Locate every uninfected red blood cell.
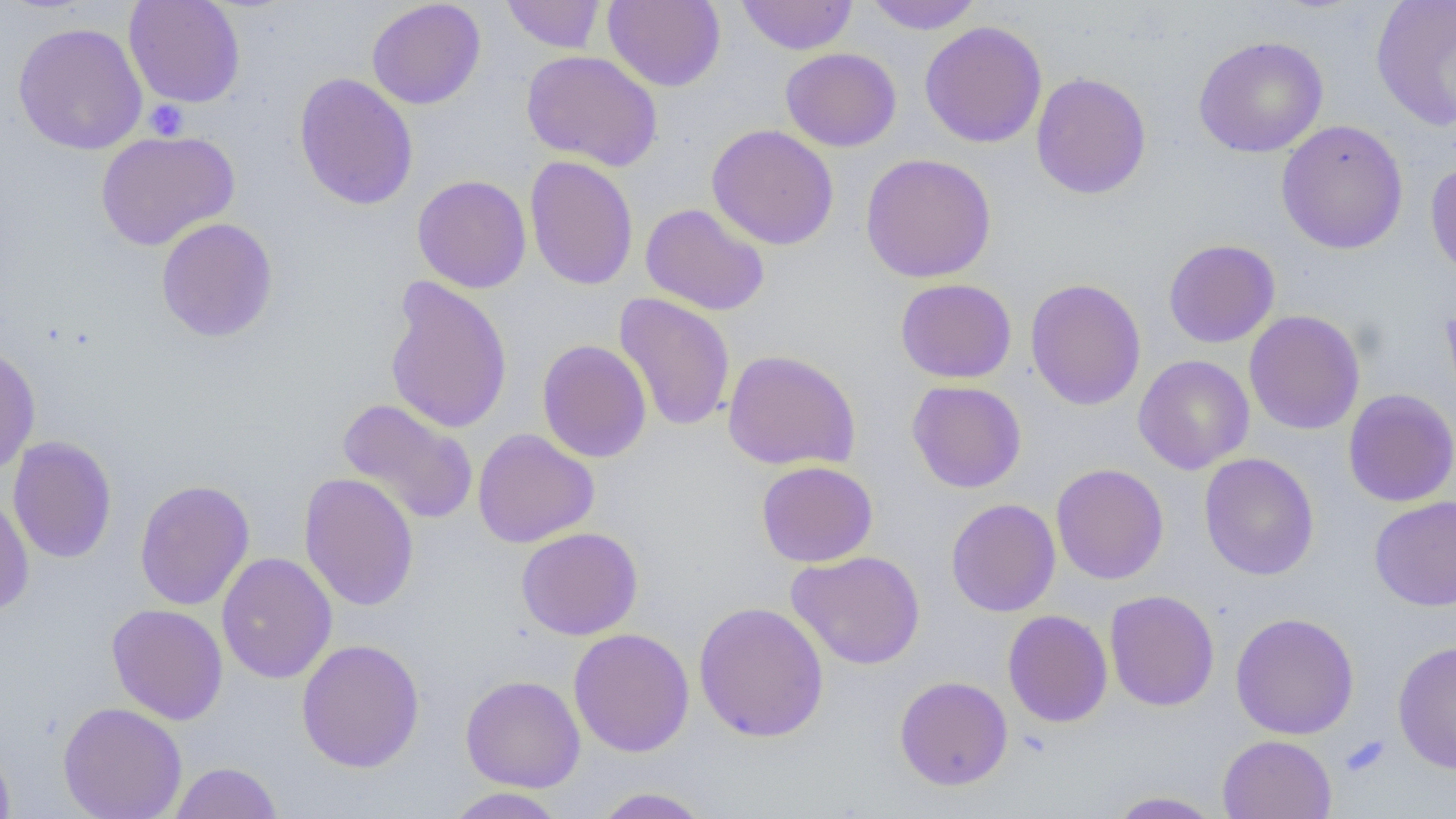
Approximate bounding boxes as (x1, y1, x2, y2) in pixels.
Uninfected red blood cells: (123, 0, 246, 108), (367, 0, 486, 110), (501, 0, 606, 53), (603, 0, 725, 91), (737, 0, 857, 55), (863, 0, 984, 34), (1370, 0, 1456, 133), (919, 20, 1047, 148), (12, 22, 148, 155), (1193, 35, 1328, 158), (780, 48, 902, 152), (521, 50, 663, 171), (1031, 71, 1152, 199), (294, 72, 419, 210), (1276, 119, 1409, 255), (707, 124, 839, 250), (95, 129, 240, 251), (859, 153, 997, 283), (524, 156, 638, 291), (1424, 160, 1456, 283), (412, 175, 531, 293), (640, 203, 771, 316), (155, 218, 279, 342), (1163, 238, 1280, 348), (384, 275, 514, 435), (895, 278, 1017, 383), (1025, 278, 1146, 410), (614, 292, 736, 432), (1244, 309, 1366, 435), (536, 339, 652, 463), (0, 345, 41, 475), (722, 349, 861, 471), (1133, 355, 1254, 474), (906, 380, 1027, 493), (1342, 389, 1456, 507), (337, 398, 479, 525), (472, 428, 599, 548), (7, 436, 118, 564), (1199, 453, 1319, 580), (756, 460, 878, 567), (1050, 463, 1169, 584), (299, 472, 419, 612), (134, 478, 255, 611), (0, 492, 35, 616), (1369, 495, 1456, 611), (946, 498, 1061, 617), (516, 527, 643, 640), (786, 550, 926, 670), (216, 552, 337, 685), (1104, 589, 1219, 711), (694, 601, 829, 742), (106, 604, 229, 725), (1003, 609, 1113, 728), (1230, 611, 1359, 740), (568, 628, 695, 757), (296, 639, 425, 772), (1393, 639, 1456, 773), (460, 675, 586, 793), (895, 675, 1013, 791), (59, 701, 187, 819), (1218, 734, 1337, 819), (0, 740, 16, 818), (169, 761, 283, 818), (442, 787, 569, 818), (589, 787, 712, 818), (1106, 791, 1225, 818).

slide_level_diagnosis: negative for blood parasites
modality: light microscopy
preparation: thin blood film
field_of_view: one of a larger specimen
image_size: 1456×819 pixels
magnification: 1000x
platelet_locations: 'approximate bounding boxes as (x1, y1, x2, y2) in pixels: (145, 100, 188, 140), (1341, 734, 1390, 778)'